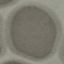

Result: no malaria parasites seen. Giemsa-stained preparation. Cell patch, automatically extracted from a larger field of view and resized to 64 × 64 pixels. Thin blood film. Photographed with a smartphone camera at the microscope eyepiece.